Comment on the morphology of the red blood cells.
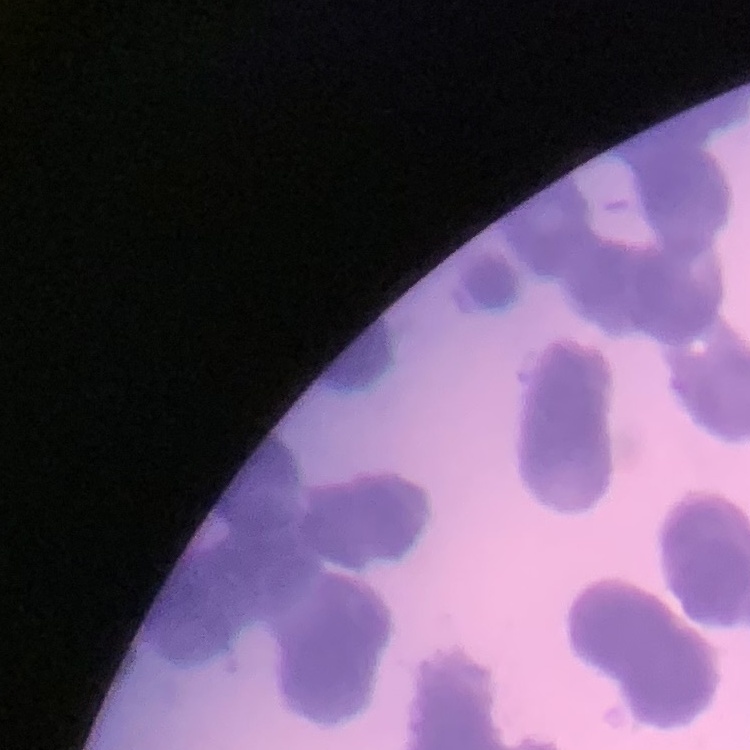

Rouleaux formation.

image type = one tile cut from a larger photomicrograph
stain = Field's or Giemsa
preparation = thin blood smear